Locate every blood parasite and identify its species.
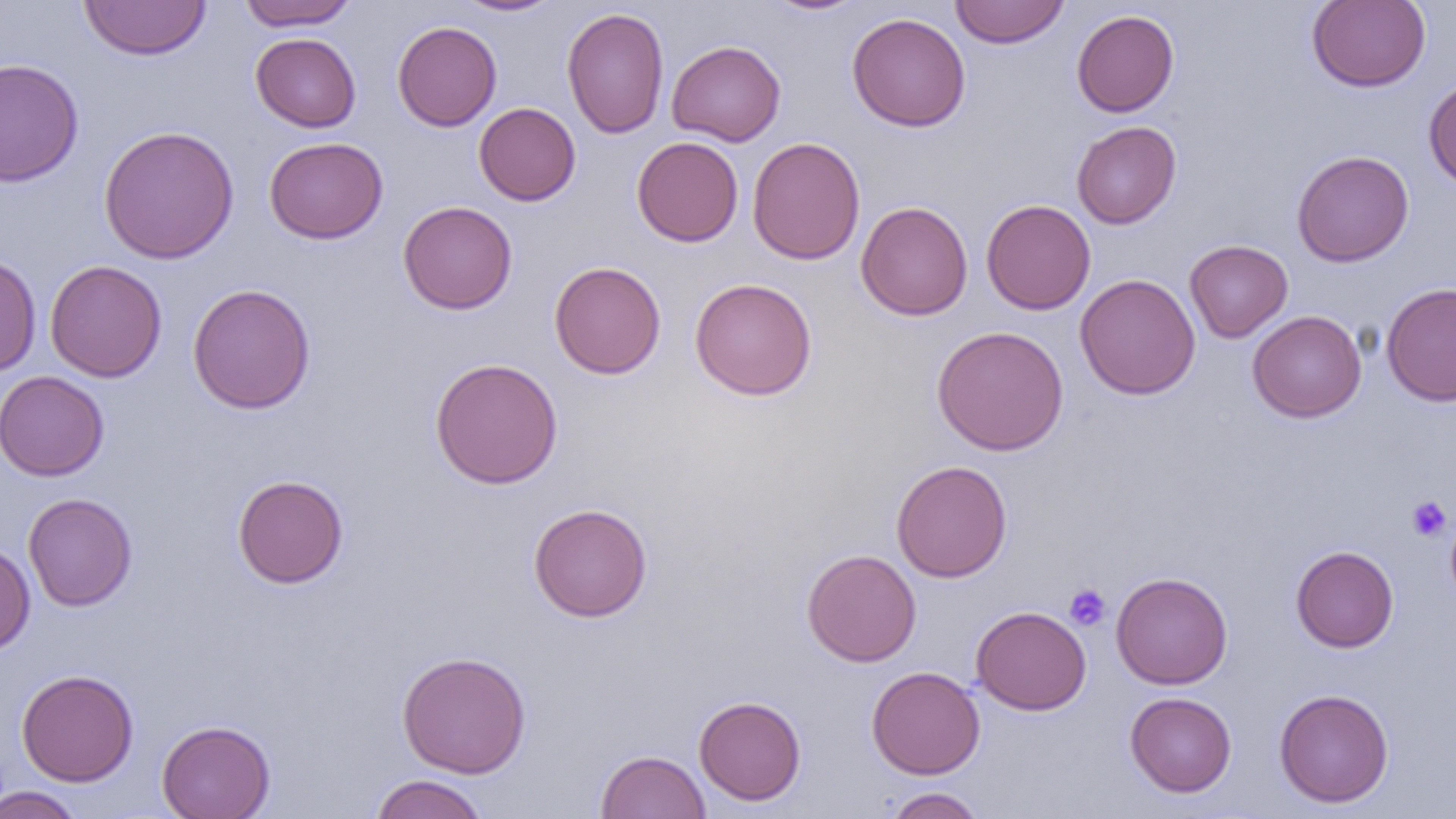
No blood parasites observed.

Approximate bounding boxes as [x1, y1, x2, y2] in pixels. Platelet locations: [1406, 496, 1452, 542], [1064, 583, 1111, 631]. Uninfected red blood cell locations: [236, 0, 358, 30], [452, 0, 565, 17], [763, 0, 870, 16], [949, 0, 1070, 48], [1307, 0, 1431, 92], [78, 1, 212, 61], [561, 7, 669, 139], [1071, 9, 1179, 117], [846, 12, 971, 132], [392, 21, 502, 131], [250, 33, 361, 132], [666, 40, 785, 147], [0, 58, 84, 187], [1423, 76, 1456, 191], [473, 102, 581, 206], [1071, 121, 1181, 229], [98, 125, 239, 265], [264, 136, 388, 244], [632, 137, 743, 247], [747, 137, 866, 265], [1291, 150, 1414, 267], [981, 199, 1096, 315], [398, 200, 518, 315], [855, 201, 973, 321], [1184, 239, 1293, 343], [0, 252, 41, 377], [44, 260, 167, 382], [549, 261, 666, 379], [1075, 273, 1200, 399], [689, 277, 817, 400], [1381, 281, 1456, 406], [187, 283, 316, 415], [1247, 310, 1366, 423], [931, 325, 1069, 456], [429, 357, 563, 489], [0, 370, 109, 481], [891, 460, 1012, 582], [232, 474, 349, 589], [23, 493, 137, 612], [528, 503, 653, 622], [1445, 506, 1456, 608], [0, 540, 36, 657], [1290, 545, 1399, 652], [802, 549, 922, 667], [1111, 571, 1233, 689], [970, 605, 1092, 715], [396, 650, 532, 778], [866, 666, 985, 779], [16, 669, 139, 786], [1273, 688, 1395, 807], [1124, 691, 1237, 797], [694, 695, 806, 806], [157, 719, 275, 819], [596, 750, 710, 819], [368, 773, 490, 819], [0, 785, 87, 819], [881, 787, 987, 818]. Slide-level diagnosis: negative for blood parasites. Single field of view. Thin blood smear. 1000x magnification. Image is 1456×819 pixels. Optical microscopy.